Give the extent of all Plasmodium vivax-infected red blood cells.
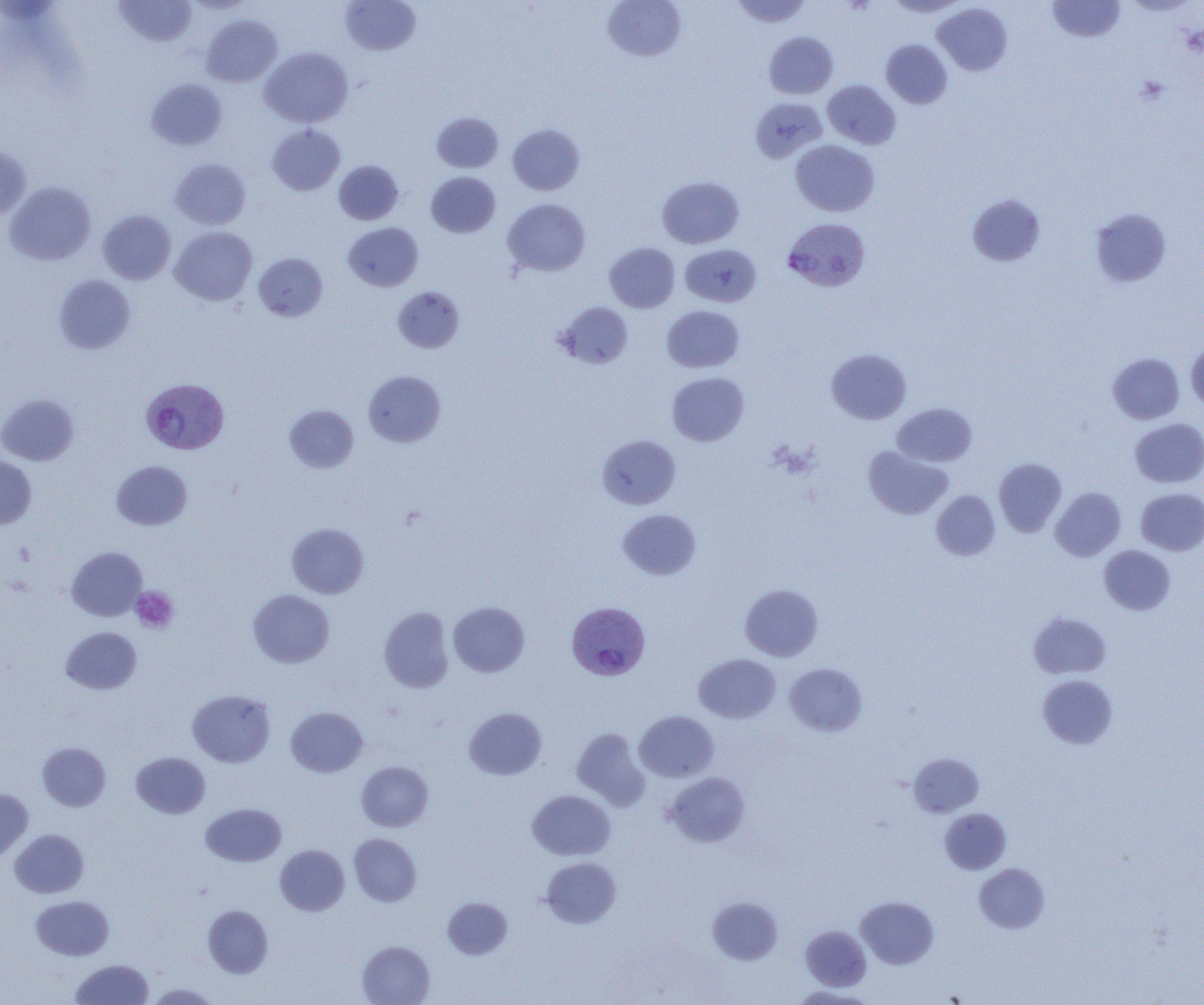

Approximate bounding boxes as named x1/y1/x2/y2 corners in pixels.
Plasmodium vivax-infected red blood cells: (x1=783, y1=218, x2=870, y2=292), (x1=145, y1=379, x2=233, y2=456), (x1=568, y1=603, x2=651, y2=682).

slide-level diagnosis = Plasmodium vivax
field of view = single
magnification = 1000x
preparation = thin blood film
uninfected red blood cell locations = approximate bounding boxes as named x1/y1/x2/y2 corners in pixels: (x1=114, y1=0, x2=197, y2=47), (x1=340, y1=0, x2=421, y2=55), (x1=602, y1=0, x2=686, y2=62), (x1=731, y1=0, x2=812, y2=27), (x1=885, y1=0, x2=968, y2=17), (x1=1047, y1=0, x2=1125, y2=42), (x1=933, y1=3, x2=1013, y2=75), (x1=201, y1=14, x2=282, y2=87), (x1=763, y1=32, x2=838, y2=99), (x1=881, y1=39, x2=952, y2=109), (x1=259, y1=47, x2=353, y2=128), (x1=146, y1=78, x2=227, y2=150), (x1=823, y1=80, x2=901, y2=149), (x1=750, y1=97, x2=827, y2=163), (x1=431, y1=112, x2=503, y2=173), (x1=267, y1=124, x2=344, y2=195), (x1=508, y1=124, x2=585, y2=195), (x1=790, y1=140, x2=879, y2=217), (x1=0, y1=146, x2=31, y2=221), (x1=170, y1=158, x2=251, y2=230), (x1=334, y1=160, x2=403, y2=224), (x1=426, y1=171, x2=500, y2=238), (x1=657, y1=176, x2=744, y2=248), (x1=4, y1=181, x2=96, y2=265), (x1=967, y1=194, x2=1046, y2=266), (x1=502, y1=198, x2=591, y2=277), (x1=1090, y1=207, x2=1172, y2=288), (x1=98, y1=210, x2=176, y2=284), (x1=343, y1=222, x2=423, y2=291), (x1=170, y1=226, x2=257, y2=305), (x1=604, y1=242, x2=680, y2=313), (x1=680, y1=244, x2=761, y2=307), (x1=254, y1=253, x2=328, y2=321), (x1=53, y1=274, x2=135, y2=354), (x1=393, y1=287, x2=464, y2=352), (x1=555, y1=302, x2=633, y2=369), (x1=662, y1=305, x2=744, y2=372), (x1=1186, y1=340, x2=1204, y2=413), (x1=826, y1=348, x2=911, y2=424), (x1=1108, y1=353, x2=1184, y2=424), (x1=363, y1=371, x2=446, y2=447), (x1=667, y1=372, x2=749, y2=446), (x1=0, y1=394, x2=79, y2=465), (x1=893, y1=402, x2=977, y2=467), (x1=284, y1=405, x2=359, y2=473), (x1=1130, y1=418, x2=1204, y2=487), (x1=597, y1=435, x2=681, y2=509), (x1=863, y1=446, x2=953, y2=520), (x1=0, y1=455, x2=37, y2=528), (x1=994, y1=458, x2=1066, y2=536), (x1=111, y1=460, x2=192, y2=530), (x1=1050, y1=487, x2=1126, y2=561), (x1=1135, y1=488, x2=1204, y2=556), (x1=931, y1=490, x2=1000, y2=561), (x1=618, y1=509, x2=700, y2=579), (x1=287, y1=523, x2=368, y2=598), (x1=1099, y1=545, x2=1175, y2=615), (x1=66, y1=546, x2=147, y2=621), (x1=740, y1=584, x2=823, y2=661), (x1=248, y1=589, x2=335, y2=668), (x1=448, y1=601, x2=530, y2=677), (x1=379, y1=607, x2=455, y2=693), (x1=1029, y1=612, x2=1111, y2=679), (x1=60, y1=626, x2=142, y2=694), (x1=694, y1=653, x2=780, y2=724), (x1=785, y1=663, x2=867, y2=736), (x1=1038, y1=674, x2=1118, y2=748), (x1=187, y1=689, x2=276, y2=767), (x1=286, y1=706, x2=368, y2=777), (x1=464, y1=707, x2=547, y2=779), (x1=634, y1=711, x2=719, y2=782), (x1=571, y1=727, x2=650, y2=810), (x1=38, y1=742, x2=110, y2=811), (x1=131, y1=752, x2=210, y2=818), (x1=908, y1=753, x2=983, y2=817), (x1=356, y1=761, x2=433, y2=832), (x1=664, y1=772, x2=750, y2=847), (x1=0, y1=790, x2=32, y2=861), (x1=527, y1=790, x2=615, y2=860), (x1=201, y1=803, x2=286, y2=867), (x1=939, y1=808, x2=1011, y2=874), (x1=10, y1=829, x2=89, y2=898), (x1=349, y1=833, x2=421, y2=906), (x1=275, y1=845, x2=349, y2=916), (x1=541, y1=857, x2=621, y2=928), (x1=974, y1=863, x2=1050, y2=933), (x1=31, y1=895, x2=114, y2=960), (x1=708, y1=896, x2=783, y2=964), (x1=856, y1=896, x2=939, y2=969), (x1=442, y1=897, x2=513, y2=959), (x1=203, y1=905, x2=273, y2=978), (x1=801, y1=926, x2=871, y2=990), (x1=357, y1=941, x2=435, y2=1005), (x1=70, y1=959, x2=154, y2=1004), (x1=147, y1=983, x2=220, y2=1004), (x1=789, y1=986, x2=878, y2=1004)
image size = 1204×1005 pixels
platelet locations = approximate bounding boxes as named x1/y1/x2/y2 corners in pixels: (x1=1136, y1=75, x2=1169, y2=105), (x1=131, y1=587, x2=178, y2=633)
modality = optical microscopy